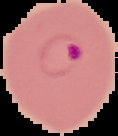
preparation: thin blood smear
image_type: segmented cell region on a black background
result: malaria parasites identified
image_size: 118×136 pixels